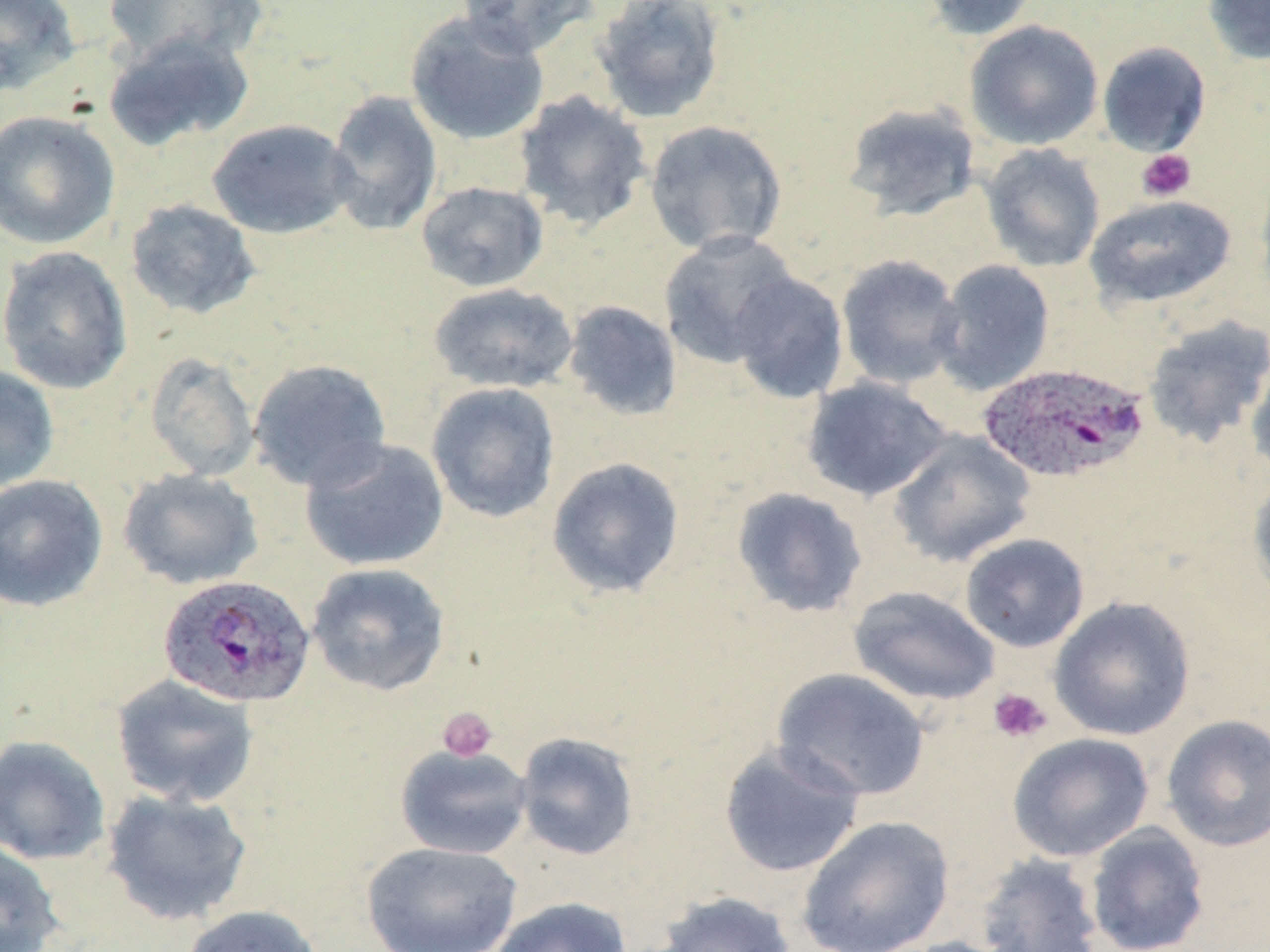
slide-level diagnosis = Plasmodium ovale
stain = May-Grünwald-Giemsa
preparation = thin blood film
uninfected red blood cell locations = approximate bounding boxes as named x1/y1/x2/y2 corners in pixels: (x1=0, y1=0, x2=81, y2=97), (x1=456, y1=0, x2=597, y2=58), (x1=591, y1=0, x2=726, y2=124), (x1=921, y1=0, x2=1041, y2=41), (x1=1202, y1=0, x2=1270, y2=66), (x1=102, y1=1, x2=268, y2=68), (x1=405, y1=10, x2=550, y2=145), (x1=964, y1=19, x2=1105, y2=151), (x1=102, y1=30, x2=255, y2=151), (x1=1097, y1=41, x2=1211, y2=156), (x1=324, y1=90, x2=443, y2=236), (x1=513, y1=90, x2=652, y2=232), (x1=842, y1=101, x2=982, y2=221), (x1=0, y1=110, x2=120, y2=250), (x1=207, y1=119, x2=357, y2=239), (x1=643, y1=119, x2=788, y2=255), (x1=980, y1=143, x2=1106, y2=272), (x1=1254, y1=169, x2=1270, y2=303), (x1=415, y1=180, x2=549, y2=293), (x1=1084, y1=194, x2=1237, y2=310), (x1=124, y1=198, x2=261, y2=320), (x1=659, y1=231, x2=801, y2=369), (x1=0, y1=246, x2=133, y2=395), (x1=836, y1=253, x2=965, y2=390), (x1=931, y1=259, x2=1055, y2=396), (x1=728, y1=271, x2=849, y2=404), (x1=428, y1=282, x2=579, y2=394), (x1=562, y1=300, x2=683, y2=421), (x1=1142, y1=315, x2=1270, y2=449), (x1=144, y1=351, x2=260, y2=482), (x1=1246, y1=355, x2=1270, y2=486), (x1=247, y1=358, x2=392, y2=492), (x1=0, y1=365, x2=60, y2=492), (x1=802, y1=376, x2=952, y2=502), (x1=425, y1=382, x2=561, y2=524), (x1=888, y1=429, x2=1036, y2=568), (x1=300, y1=436, x2=449, y2=571), (x1=546, y1=456, x2=686, y2=599), (x1=118, y1=468, x2=263, y2=590), (x1=0, y1=474, x2=109, y2=612), (x1=1247, y1=475, x2=1270, y2=602), (x1=731, y1=487, x2=868, y2=618), (x1=959, y1=533, x2=1090, y2=653), (x1=306, y1=562, x2=451, y2=696), (x1=848, y1=585, x2=1001, y2=707), (x1=1049, y1=596, x2=1196, y2=741), (x1=771, y1=667, x2=931, y2=801), (x1=111, y1=674, x2=260, y2=808), (x1=1160, y1=713, x2=1270, y2=852), (x1=514, y1=731, x2=640, y2=860), (x1=1007, y1=732, x2=1154, y2=862), (x1=0, y1=735, x2=111, y2=865), (x1=718, y1=742, x2=866, y2=878), (x1=395, y1=743, x2=533, y2=860), (x1=101, y1=788, x2=253, y2=926), (x1=797, y1=815, x2=955, y2=952), (x1=1084, y1=823, x2=1210, y2=952), (x1=0, y1=840, x2=64, y2=952), (x1=361, y1=841, x2=523, y2=952), (x1=975, y1=852, x2=1104, y2=952), (x1=654, y1=891, x2=798, y2=952), (x1=489, y1=896, x2=631, y2=952), (x1=180, y1=904, x2=325, y2=952), (x1=891, y1=936, x2=1023, y2=952)
modality = optical microscopy
Plasmodium ovale-infected red blood cell locations = approximate bounding boxes as named x1/y1/x2/y2 corners in pixels: (x1=977, y1=361, x2=1149, y2=484), (x1=158, y1=574, x2=316, y2=709)
magnification = 1000x
platelet locations = approximate bounding boxes as named x1/y1/x2/y2 corners in pixels: (x1=1136, y1=149, x2=1196, y2=202), (x1=988, y1=687, x2=1052, y2=743), (x1=438, y1=706, x2=498, y2=762)
field of view = one of a larger specimen
image size = 1270×952 pixels